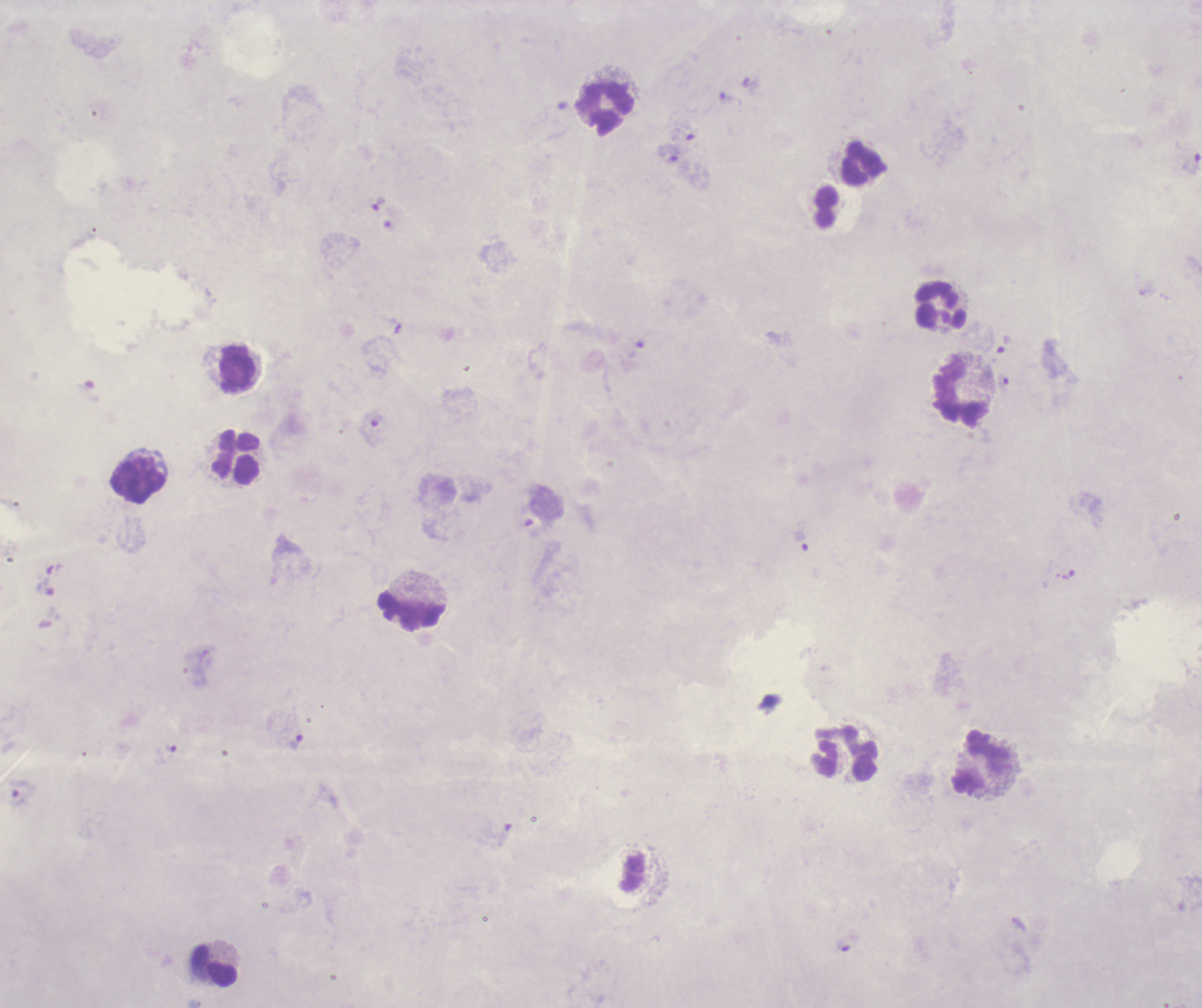

Approximate centers as (x, y) in pixels.
Summary:
  - Leukocyte locations: (607, 107), (863, 161), (940, 306), (238, 368), (958, 390), (238, 458), (138, 480), (412, 610), (847, 755), (981, 763), (216, 965)
  - Trophozoite locations: (726, 98), (670, 154), (1190, 163), (380, 205), (1003, 344), (372, 429), (801, 541), (46, 588), (295, 741), (167, 753), (843, 946)
  - Background quality: poor
  - Preparation: thick smear of blood
  - Field of view: single
  - Image size: 1202×1008 pixels
  - Stain: Romanowsky
  - Context: previously used in an actual diagnosis
  - Result: malaria parasites detected
  - Magnification: 100x
  - Coloration quality: bad